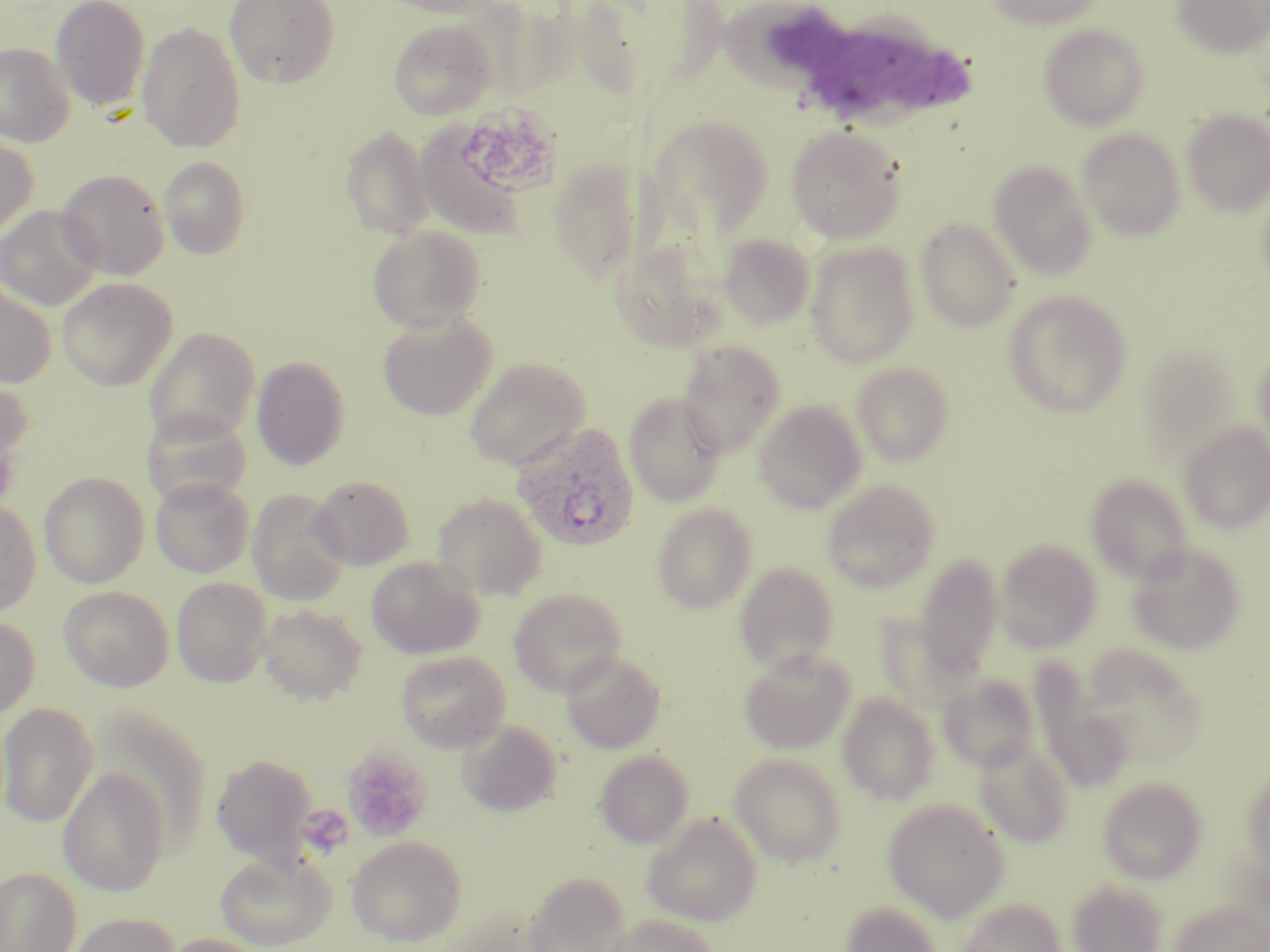
Summary:
  - Coordinate format: approximate bounding boxes as [x1, y1, x2, y2] in pixels
  - Platelet locations: [471, 103, 561, 192], [342, 746, 432, 842]
  - Uninfected red blood cell locations (subset): [51, 0, 150, 110], [225, 0, 340, 89], [375, 0, 503, 18], [986, 0, 1111, 30], [1172, 0, 1270, 59], [719, 9, 844, 97], [388, 19, 496, 120], [137, 22, 246, 152], [1038, 25, 1149, 130], [0, 42, 75, 147], [1181, 109, 1270, 217], [785, 125, 905, 243], [339, 126, 435, 241], [1078, 128, 1185, 240], [0, 135, 39, 239], [159, 156, 250, 259], [546, 158, 647, 284], [989, 160, 1097, 279], [55, 168, 170, 280], [0, 205, 102, 310], [915, 218, 1020, 333], [368, 225, 487, 333], [720, 234, 815, 330], [805, 242, 919, 368], [57, 277, 177, 391], [0, 283, 56, 388], [1003, 290, 1132, 418], [379, 311, 497, 420], [144, 327, 260, 443], [678, 340, 786, 457], [1136, 345, 1245, 467], [1253, 345, 1270, 461], [252, 357, 349, 470], [464, 357, 590, 469], [852, 361, 954, 466], [0, 375, 34, 479], [624, 393, 726, 507], [753, 401, 867, 513], [142, 409, 252, 507], [1179, 421, 1270, 534], [39, 471, 149, 588], [1085, 473, 1193, 584], [310, 475, 415, 570], [150, 476, 254, 578], [822, 478, 941, 592], [247, 489, 350, 605], [433, 492, 548, 600], [0, 500, 42, 617], [652, 503, 758, 614], [995, 539, 1102, 652], [1127, 543, 1246, 655], [914, 554, 1004, 678], [366, 556, 484, 659], [734, 561, 840, 675], [171, 577, 272, 687], [59, 585, 174, 691], [509, 587, 627, 696], [257, 602, 368, 705], [0, 616, 40, 720], [1081, 647, 1207, 768], [738, 648, 855, 754], [396, 649, 511, 752], [561, 651, 667, 755], [1032, 671, 1134, 793], [938, 673, 1040, 771], [837, 693, 940, 806], [0, 702, 98, 828], [457, 720, 562, 816], [974, 739, 1073, 848], [595, 750, 694, 848], [729, 753, 847, 867], [211, 754, 318, 866], [58, 768, 171, 896], [1243, 769, 1270, 866], [1098, 777, 1207, 884], [883, 798, 1010, 922], [642, 811, 763, 926], [347, 836, 467, 947], [214, 850, 336, 951], [0, 866, 82, 952], [523, 871, 633, 952], [1067, 880, 1169, 952], [958, 898, 1067, 952], [1168, 899, 1270, 952], [839, 900, 942, 952], [67, 913, 181, 952], [606, 914, 719, 952], [159, 934, 270, 952]
  - Plasmodium ovale-infected red blood cell locations (subset): [510, 421, 639, 552]
  - Slide-level diagnosis: Plasmodium ovale
  - Preparation: thin blood film
  - Stain: May-Grünwald-Giemsa
  - Field of view: single
  - Image size: 1270×952 pixels
  - Magnification: 1000x
  - Modality: optical microscopy